Report the malaria status of this cell.
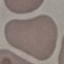

Uninfected.

Summary:
  - Preparation: thin smear
  - Stain: Giemsa
  - Image type: automatically extracted cell patch, resized to 64 × 64 pixels
  - Capture: smartphone through the microscope eyepiece